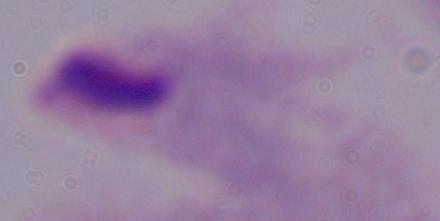
A trichomonad is shown. Photomicrograph. Captured at 1000x magnification.